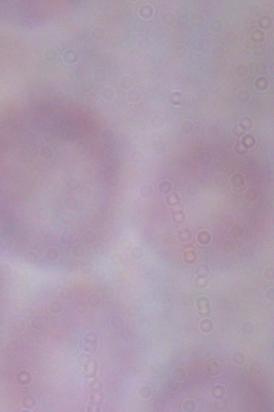
A trypanosome is shown. Captured at 1000x magnification. Photomicrograph.